Give the extent of all Plasmodium ovale-infected red blood cells.
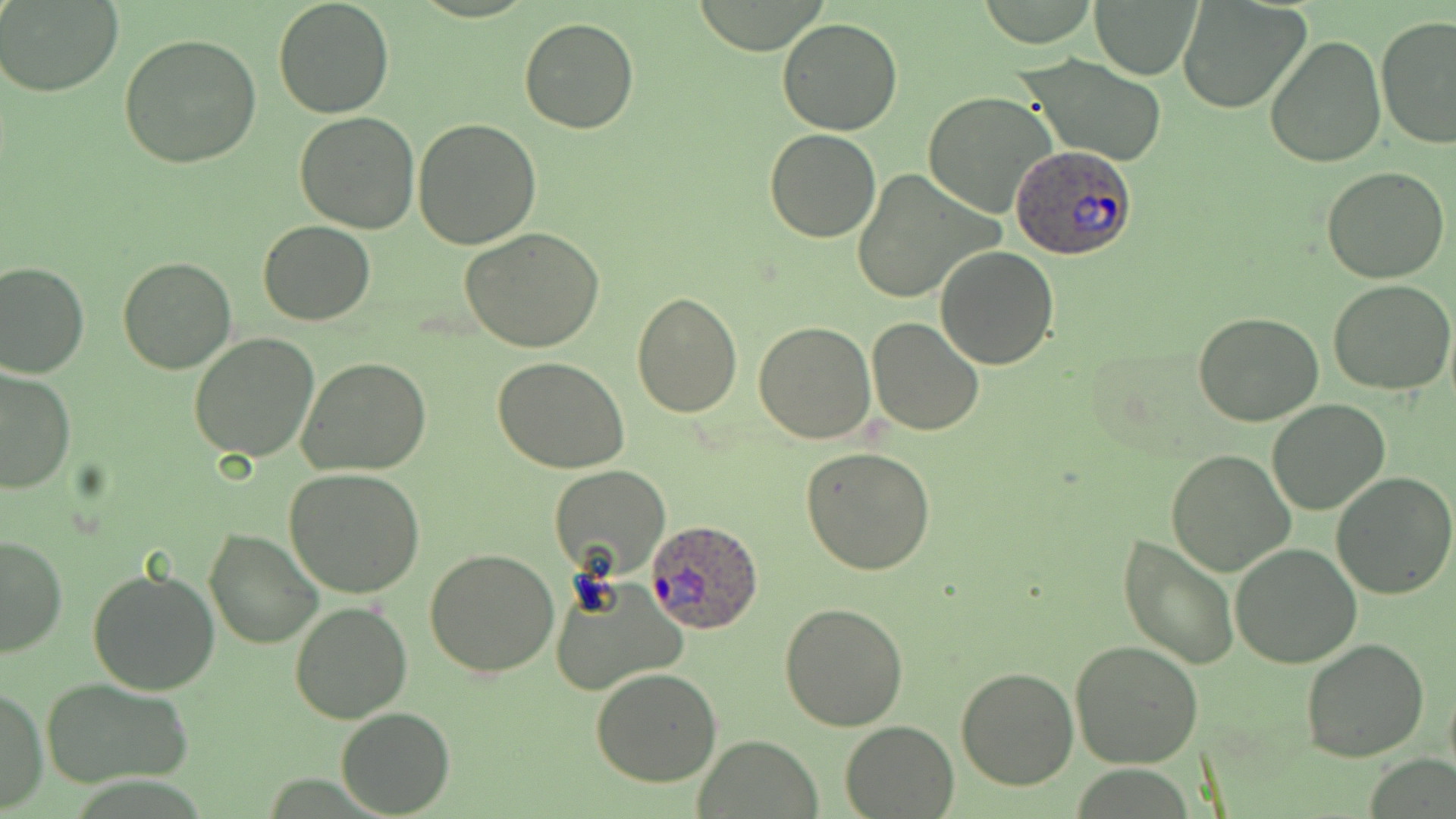

Approximate bounding boxes as (x1, y1, x2, y2) in pixels.
Plasmodium ovale-infected red blood cells: (1012, 144, 1136, 259), (646, 518, 763, 632).

{
  "slide_level_diagnosis": "Plasmodium ovale",
  "field_of_view": "single",
  "uninfected_red_blood_cell_locations": "approximate bounding boxes as (x1, y1, x2, y2) in pixels: (273, 0, 395, 118), (1090, 0, 1204, 80), (1176, 0, 1311, 115), (0, 1, 124, 97), (1376, 16, 1456, 153), (776, 17, 906, 135), (517, 19, 639, 135), (119, 32, 263, 168), (1265, 34, 1386, 168), (1016, 52, 1170, 167), (923, 91, 1058, 219), (295, 109, 420, 232), (413, 119, 543, 249), (764, 128, 883, 243), (1320, 166, 1451, 283), (852, 168, 996, 302), (258, 220, 376, 326), (461, 230, 607, 352), (935, 246, 1059, 369), (117, 254, 236, 374), (0, 260, 90, 378), (1329, 280, 1456, 397), (630, 290, 741, 418), (1193, 312, 1323, 426), (866, 317, 983, 437), (753, 319, 875, 444), (189, 333, 320, 462), (297, 357, 432, 477), (494, 357, 629, 475), (1, 367, 75, 495), (1268, 399, 1389, 515), (800, 448, 935, 575), (1166, 449, 1296, 575), (550, 466, 671, 582), (284, 469, 425, 597), (1331, 470, 1456, 598), (204, 527, 324, 648), (1117, 531, 1240, 670), (0, 535, 68, 660), (1229, 543, 1362, 667), (426, 547, 559, 678), (87, 568, 221, 697), (553, 578, 689, 695), (290, 602, 412, 724), (779, 603, 909, 732), (1300, 637, 1429, 763), (1070, 640, 1205, 771), (954, 667, 1078, 790), (590, 668, 722, 787), (41, 677, 193, 789), (0, 686, 47, 812), (336, 707, 455, 816), (840, 719, 960, 818), (694, 736, 823, 818)",
  "preparation": "thin blood film",
  "image_size": "1456×819 pixels",
  "magnification": "1000x",
  "modality": "optical microscopy",
  "stain": "May-Grünwald-Giemsa"
}